Name the parasite shown.
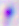

Toxoplasma gondii.

Summary:
  - Magnification: 400x
  - Modality: micrograph